Report the malaria status of this cell.
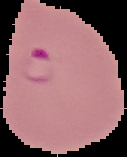
Parasitized.

image size = 127×157 pixels
image type = cell region segmented out of the field of view; surrounding area masked to black
preparation = thin blood smear